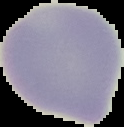
Cell region segmented out of the field of view; the surrounding area is masked to black. From a thin blood smear. Result: no malaria parasites seen. Image is 124×127 pixels.